Assess this cell for malaria.
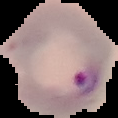
Parasitized.

{
  "image_size": "118×118 pixels",
  "preparation": "thin blood film",
  "image_type": "cell region segmented out of the field of view; surrounding area masked to black"
}